Report the malaria status of this cell.
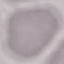

It is uninfected.

Acquired by smartphone through the microscope eyepiece. Automatically extracted cell patch, resized to 64 × 64 pixels. Thin blood smear. Giemsa-stained preparation.